Describe the morphology of the red blood cells.
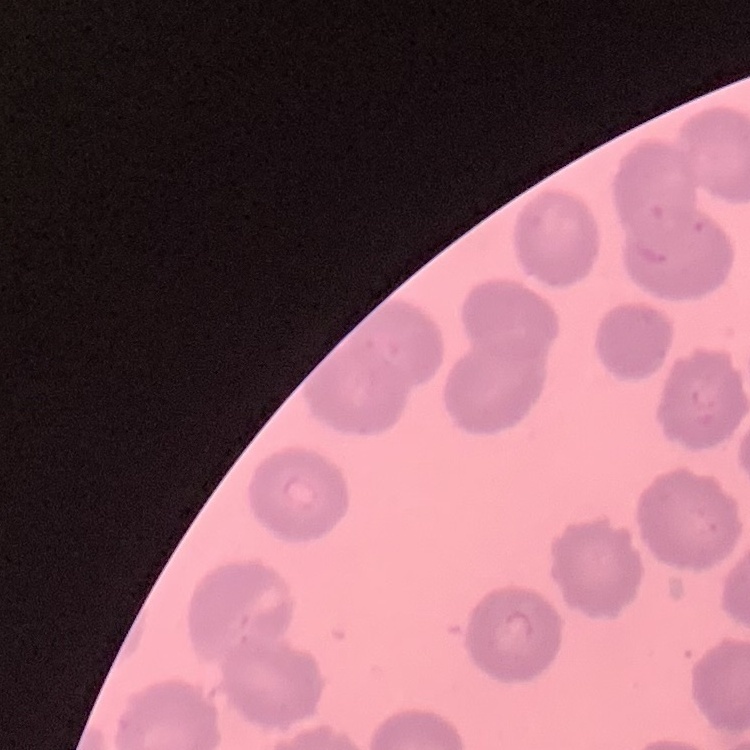

They show no rouleaux formation.

preparation: thin blood film
image_type: one tile cut from a larger photomicrograph
stain: Field's or Giemsa